Outline each blood parasite and name the species.
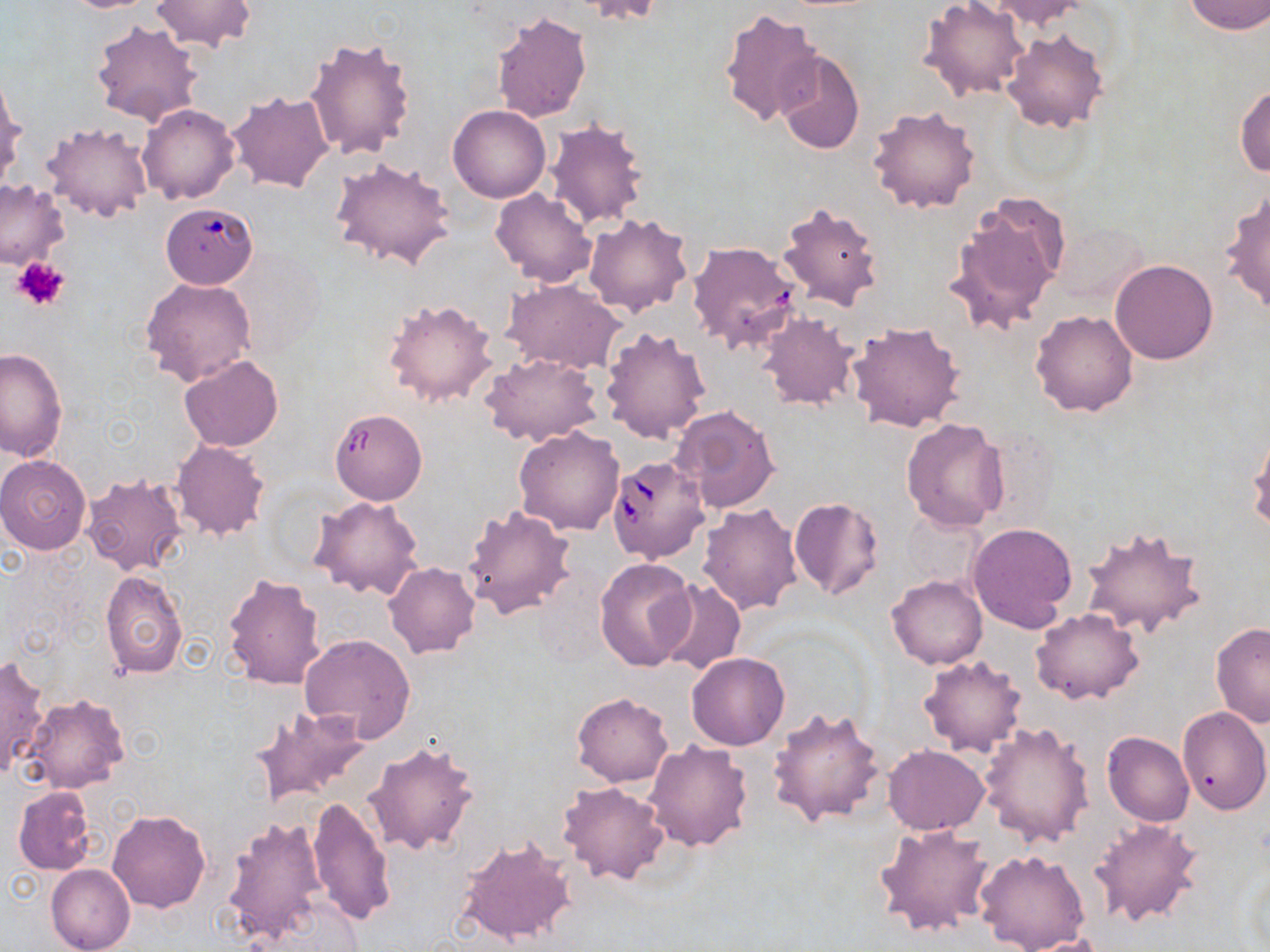
Approximate bounding boxes as named x1/y1/x2/y2 corners in pixels.
Babesia divergens-infected red blood cells: (x1=605, y1=455, x2=708, y2=563).
No Plasmodium falciparum, Plasmodium ovale, Plasmodium malariae, Plasmodium vivax, or Trypanosoma brucei observed.

Platelet locations: (x1=10, y1=257, x2=70, y2=311). Uninfected red blood cell locations: (x1=56, y1=0, x2=161, y2=12), (x1=988, y1=0, x2=1088, y2=31), (x1=150, y1=1, x2=258, y2=53), (x1=1181, y1=1, x2=1269, y2=35), (x1=918, y1=2, x2=1031, y2=101), (x1=718, y1=9, x2=825, y2=128), (x1=491, y1=12, x2=592, y2=124), (x1=90, y1=18, x2=202, y2=127), (x1=1000, y1=27, x2=1109, y2=134), (x1=304, y1=35, x2=416, y2=162), (x1=775, y1=50, x2=865, y2=155), (x1=0, y1=72, x2=24, y2=189), (x1=1234, y1=84, x2=1270, y2=179), (x1=227, y1=89, x2=335, y2=193), (x1=137, y1=104, x2=239, y2=205), (x1=867, y1=104, x2=981, y2=214), (x1=448, y1=105, x2=550, y2=203), (x1=545, y1=118, x2=650, y2=230), (x1=41, y1=121, x2=155, y2=222), (x1=329, y1=156, x2=456, y2=273), (x1=0, y1=179, x2=69, y2=270), (x1=490, y1=187, x2=597, y2=288), (x1=1221, y1=187, x2=1270, y2=317), (x1=944, y1=195, x2=1070, y2=335), (x1=777, y1=201, x2=884, y2=312), (x1=165, y1=208, x2=263, y2=290), (x1=583, y1=212, x2=694, y2=317), (x1=1057, y1=222, x2=1148, y2=305), (x1=688, y1=239, x2=803, y2=355), (x1=1109, y1=259, x2=1218, y2=364), (x1=140, y1=276, x2=255, y2=385), (x1=502, y1=279, x2=624, y2=374), (x1=383, y1=298, x2=498, y2=408), (x1=1030, y1=310, x2=1139, y2=416), (x1=756, y1=311, x2=858, y2=411), (x1=848, y1=320, x2=968, y2=432), (x1=599, y1=326, x2=712, y2=445), (x1=1, y1=346, x2=68, y2=460), (x1=482, y1=352, x2=603, y2=445), (x1=180, y1=355, x2=284, y2=451), (x1=671, y1=404, x2=781, y2=512), (x1=333, y1=412, x2=429, y2=507), (x1=900, y1=417, x2=1008, y2=534), (x1=513, y1=426, x2=624, y2=536), (x1=1247, y1=428, x2=1270, y2=535), (x1=984, y1=430, x2=1060, y2=524), (x1=171, y1=439, x2=270, y2=540), (x1=0, y1=455, x2=91, y2=554), (x1=81, y1=473, x2=188, y2=577), (x1=311, y1=495, x2=425, y2=599), (x1=788, y1=496, x2=885, y2=601), (x1=697, y1=502, x2=805, y2=617), (x1=461, y1=505, x2=576, y2=621), (x1=899, y1=510, x2=983, y2=589), (x1=967, y1=522, x2=1079, y2=633), (x1=1078, y1=523, x2=1209, y2=640), (x1=595, y1=557, x2=696, y2=670), (x1=383, y1=561, x2=481, y2=659), (x1=99, y1=570, x2=188, y2=678), (x1=221, y1=571, x2=327, y2=689), (x1=886, y1=575, x2=989, y2=670), (x1=655, y1=579, x2=746, y2=676), (x1=1031, y1=608, x2=1143, y2=704), (x1=1210, y1=623, x2=1270, y2=729), (x1=299, y1=634, x2=416, y2=742), (x1=687, y1=653, x2=790, y2=751), (x1=917, y1=654, x2=1028, y2=758), (x1=0, y1=655, x2=48, y2=778), (x1=22, y1=692, x2=130, y2=794), (x1=571, y1=692, x2=674, y2=787), (x1=249, y1=704, x2=372, y2=806), (x1=768, y1=706, x2=886, y2=828), (x1=1178, y1=706, x2=1270, y2=815), (x1=980, y1=723, x2=1094, y2=847), (x1=1102, y1=732, x2=1193, y2=827), (x1=643, y1=739, x2=755, y2=852), (x1=363, y1=740, x2=480, y2=857), (x1=883, y1=744, x2=990, y2=835), (x1=558, y1=781, x2=669, y2=885), (x1=13, y1=785, x2=96, y2=875), (x1=305, y1=796, x2=397, y2=928), (x1=107, y1=808, x2=211, y2=913), (x1=222, y1=815, x2=327, y2=946), (x1=1090, y1=816, x2=1204, y2=930), (x1=875, y1=824, x2=995, y2=938), (x1=455, y1=835, x2=578, y2=947), (x1=975, y1=849, x2=1092, y2=952), (x1=47, y1=864, x2=135, y2=952), (x1=1012, y1=933, x2=1110, y2=951). Slide-level diagnosis: Babesia divergens. Light microscopy. One field of a larger specimen. Thin blood film. 1000x magnification. Image is 1270×952 pixels. May-Grünwald-Giemsa stain.